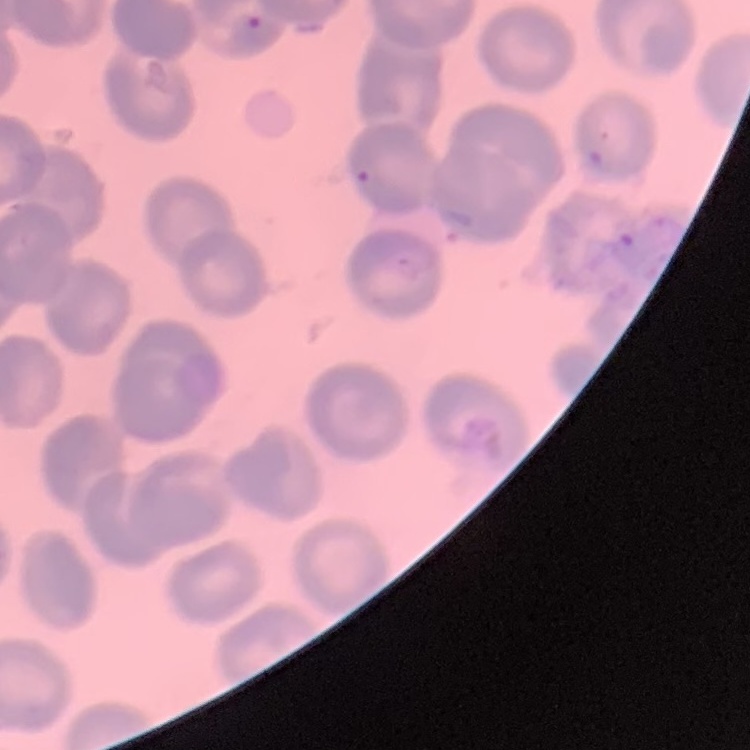 The erythrocytes exhibit no rouleaux formation. Square crop of a larger photomicrograph. Field's or Giemsa stain. Thin blood film.